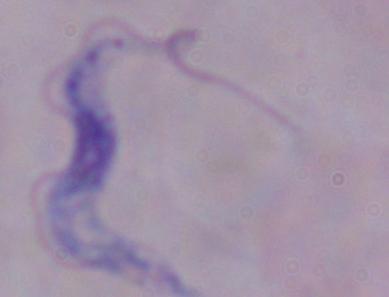
A trypanosome is shown. 1000x magnification. Micrograph.